Assess the morphology of the red blood cells.
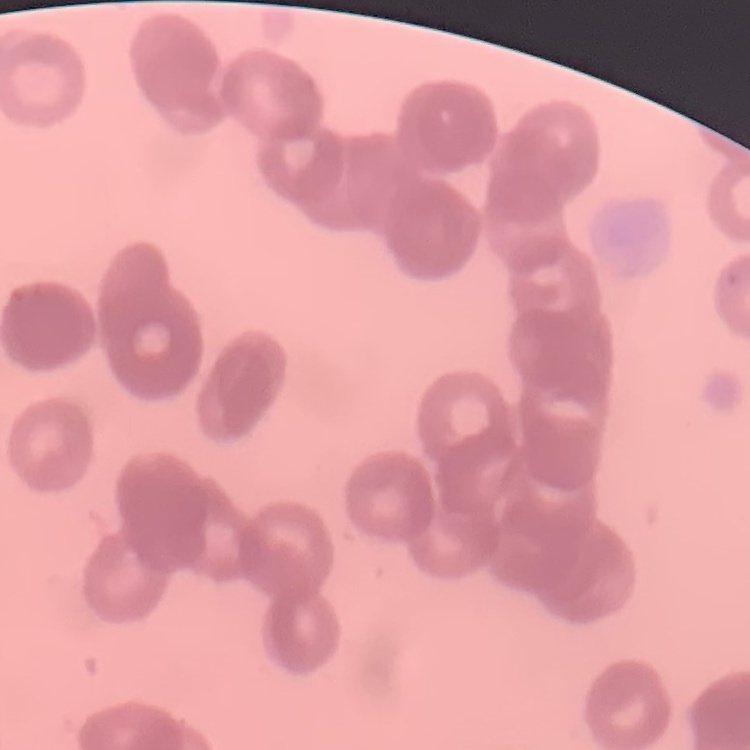

They show rouleaux formation.

One tile cut from a larger photomicrograph. Field's or Giemsa stain. Thin blood smear.